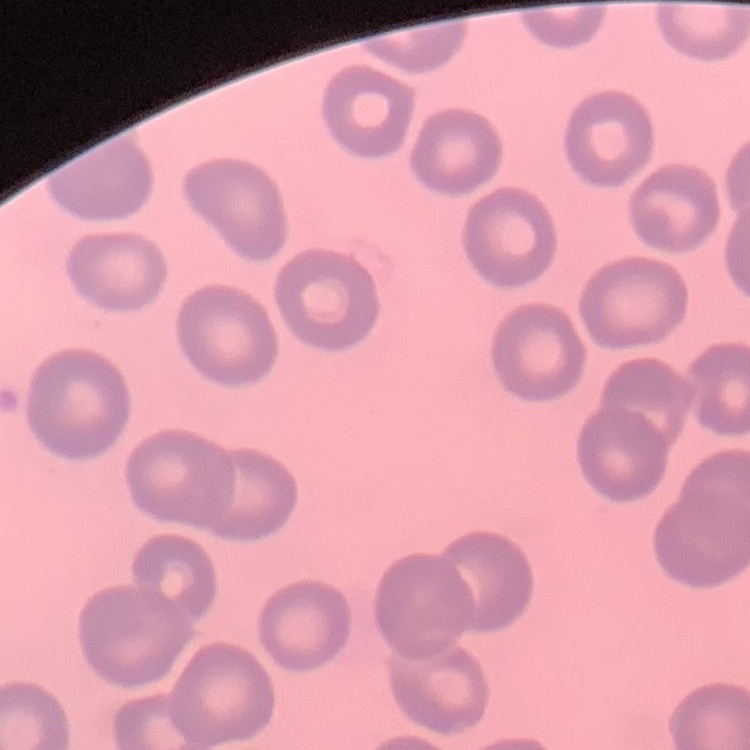
Summary:
  - Red blood cell morphology: no rouleaux formation
  - Preparation: thin blood film
  - Image type: square crop of a larger photomicrograph
  - Stain: Field's or Giemsa